Classify this cell by malaria status.
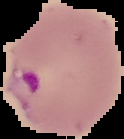

It is parasitized.

Image is 124×139 pixels. From a thin blood film. The area outside the segmented cell region is set to black.